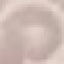

Result: no malaria parasites detected. Thin blood film. Acquired by smartphone through the microscope eyepiece. Giemsa stain. Cell patch, automatically extracted from a larger field of view and resized to 64 × 64 pixels.